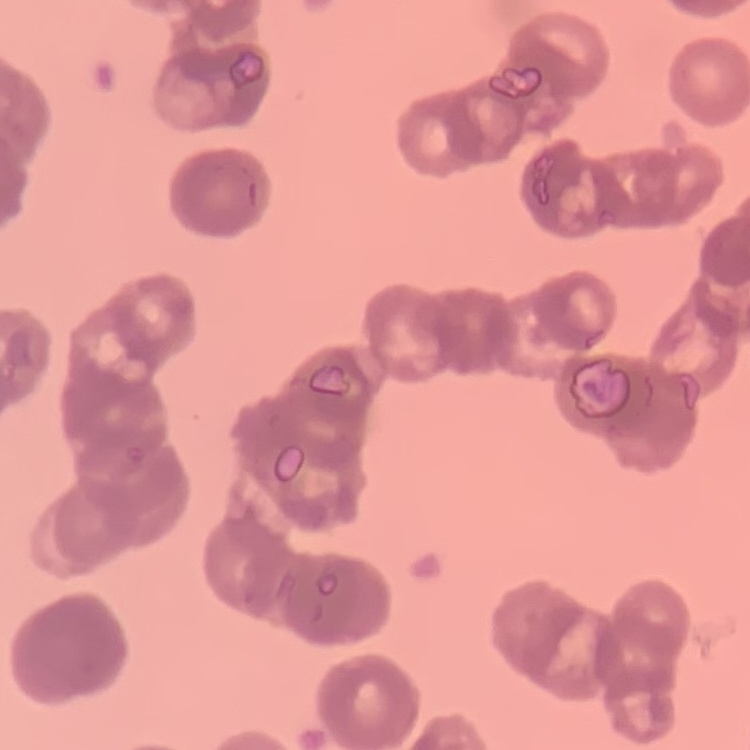

red blood cell morphology = rouleaux formation
stain = Field's or Giemsa
image type = one tile cut from a larger photomicrograph
preparation = thin blood film